State the blood parasite species.
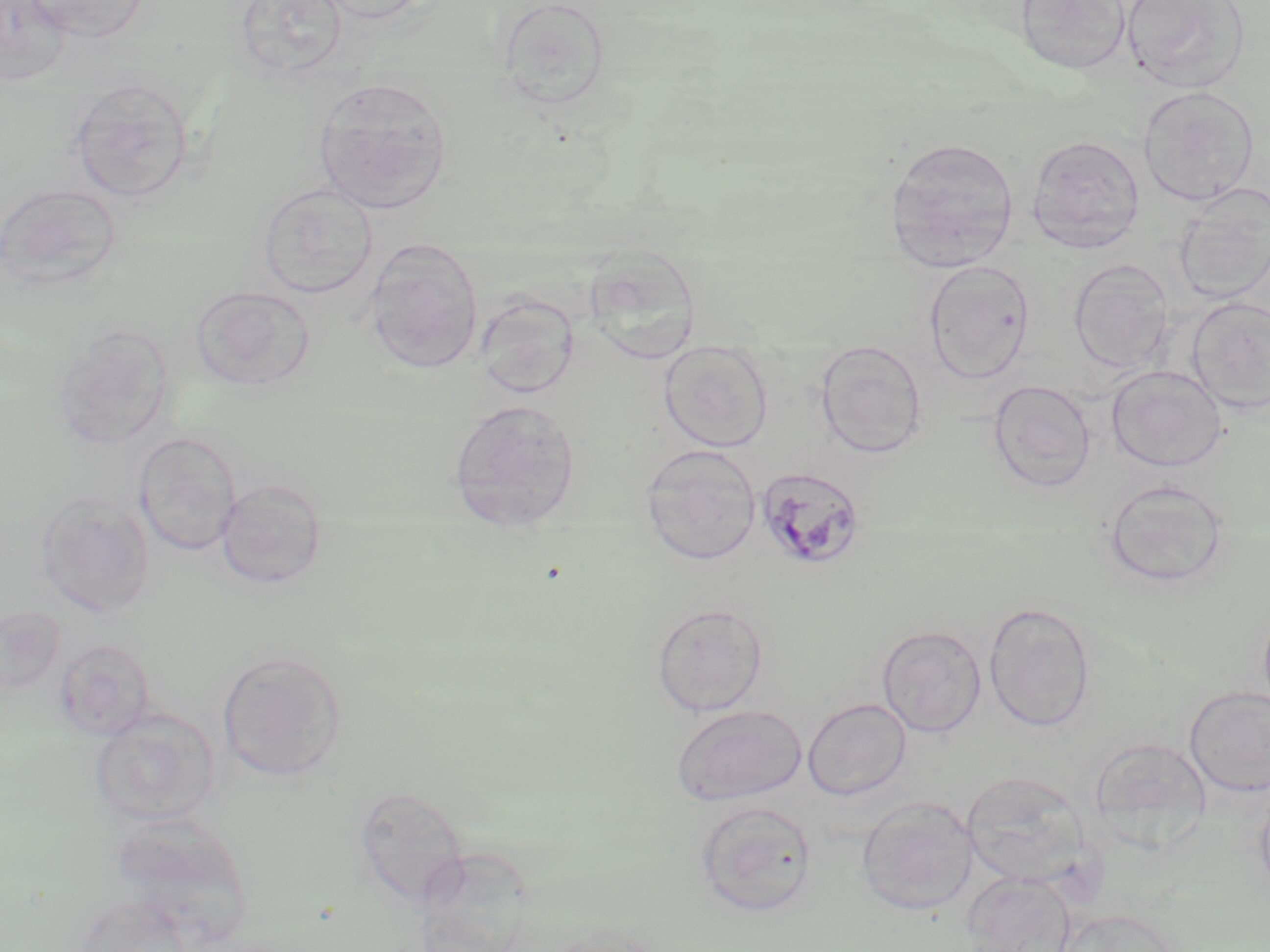
Plasmodium malariae.

{
  "uninfected_red_blood_cell_locations": "approximate bounding boxes as (x1, y1, x2, y2) in pixels: (0, 0, 74, 87), (25, 0, 149, 42), (235, 0, 349, 81), (311, 0, 435, 23), (1014, 0, 1131, 77), (1121, 0, 1249, 92), (497, 1, 611, 111), (313, 77, 451, 214), (68, 78, 197, 203), (1137, 85, 1259, 205), (1026, 134, 1146, 253), (884, 136, 1020, 270), (0, 183, 122, 290), (259, 183, 378, 299), (1173, 185, 1270, 305), (364, 238, 484, 374), (582, 245, 703, 365), (923, 259, 1035, 382), (1069, 259, 1174, 374), (190, 286, 314, 390), (474, 292, 580, 398), (1187, 297, 1270, 414), (52, 324, 174, 451), (814, 339, 928, 458), (659, 341, 773, 452), (1106, 365, 1226, 471), (987, 379, 1097, 493), (449, 399, 581, 532), (134, 431, 242, 555), (641, 445, 761, 565), (215, 478, 327, 588), (1105, 478, 1228, 587), (35, 492, 154, 618), (983, 601, 1095, 731), (651, 602, 768, 717), (0, 604, 66, 695), (877, 625, 987, 737), (53, 638, 156, 740), (217, 650, 348, 781), (1183, 686, 1270, 797), (803, 698, 911, 800), (671, 703, 808, 805), (90, 707, 220, 828), (1088, 735, 1214, 852), (961, 770, 1093, 887), (1255, 785, 1270, 903), (856, 796, 978, 916), (694, 800, 817, 917), (110, 813, 249, 946), (962, 871, 1076, 952)",
  "stain": "May-Grünwald-Giemsa",
  "modality": "optical microscopy",
  "plasmodium_malariae_infected_red_blood_cell_locations": "approximate bounding boxes as (x1, y1, x2, y2) in pixels: (755, 465, 866, 571)",
  "image_size": "1270×952 pixels",
  "preparation": "thin blood smear",
  "magnification": "1000x",
  "field_of_view": "single"
}